Classify this cell by malaria status.
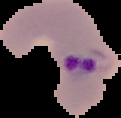
It is parasitized.

{
  "preparation": "thin blood smear",
  "image_type": "cell region segmented out of the field of view; surrounding area masked to black",
  "image_size": "121×118 pixels"
}